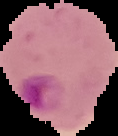

Summary:
  - Image size: 118×136 pixels
  - Image type: cell region segmented out of the field of view; surrounding area masked to black
  - Preparation: thin blood film
  - Malaria status: parasitized